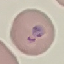

{
  "result": "malaria parasites identified",
  "capture": "smartphone camera at the microscope eyepiece",
  "stain": "Giemsa",
  "image_type": "cell patch, automatically extracted from a larger field of view and resized to 64 × 64 pixels",
  "preparation": "thin blood film"
}